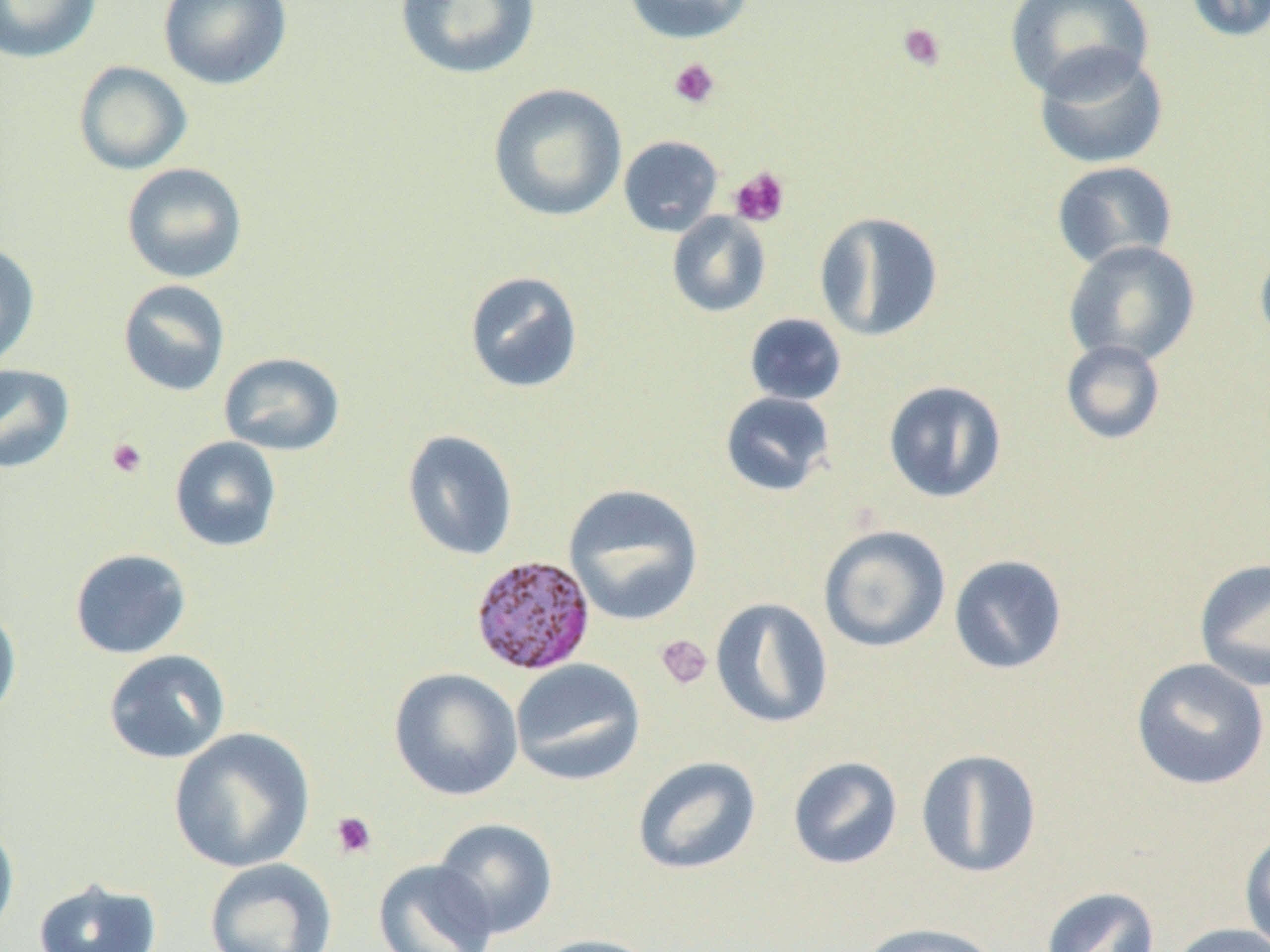
slide-level diagnosis = Plasmodium malariae
magnification = 1000x
image size = 1270×952 pixels
uninfected red blood cell locations = approximate bounding boxes as [x1, y1, x2, y2] in pixels: [0, 0, 101, 63], [158, 0, 292, 91], [394, 0, 540, 80], [622, 0, 757, 44], [1004, 0, 1154, 100], [1184, 0, 1270, 43], [1032, 46, 1169, 170], [73, 61, 192, 175], [488, 83, 627, 223], [618, 135, 724, 237], [1051, 161, 1179, 270], [121, 163, 248, 283], [666, 211, 772, 317], [813, 211, 944, 342], [1254, 239, 1270, 353], [1063, 240, 1200, 367], [0, 242, 40, 368], [463, 270, 584, 394], [118, 279, 231, 396], [744, 313, 847, 406], [1060, 339, 1166, 445], [218, 351, 345, 456], [0, 364, 75, 474], [883, 380, 1008, 504], [719, 391, 835, 497], [402, 430, 518, 561], [169, 436, 283, 552], [563, 483, 705, 626], [818, 524, 951, 653], [69, 548, 192, 659], [948, 555, 1068, 675], [1193, 557, 1270, 692], [710, 597, 834, 729], [0, 603, 22, 723], [103, 649, 231, 764], [1131, 657, 1270, 791], [510, 658, 645, 786], [388, 668, 523, 801], [167, 727, 316, 873], [915, 748, 1042, 879], [632, 755, 762, 875], [787, 756, 903, 870], [0, 815, 20, 944], [432, 817, 558, 938], [1239, 829, 1270, 951], [203, 858, 338, 952], [373, 858, 500, 952], [33, 877, 162, 952], [1040, 886, 1160, 952], [858, 921, 1004, 952], [1167, 923, 1270, 952], [530, 934, 665, 952]
platelet locations = approximate bounding boxes as [x1, y1, x2, y2] in pixels: [897, 22, 947, 72], [668, 58, 720, 109], [729, 166, 791, 227], [106, 438, 148, 478], [655, 634, 712, 690], [329, 811, 377, 859]
preparation = thin blood smear
Plasmodium malariae-infected red blood cell locations = approximate bounding boxes as [x1, y1, x2, y2] in pixels: [470, 554, 597, 676]
field of view = single
modality = optical microscopy